Classify this cell by malaria status.
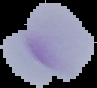
It is parasitized.

image size = 97×88 pixels
preparation = thin blood film
image type = segmented cell region with the area outside set to black